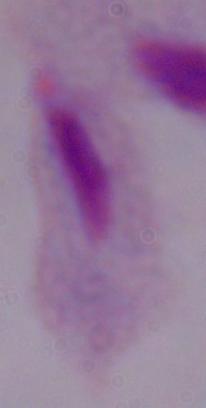
Photomicrograph. 1000x magnification. A trichomonad is seen.